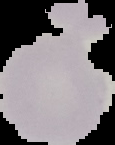

Image is 115×145 pixels. Malaria status: uninfected. The area outside the segmented cell region is set to black. From a thin blood smear.